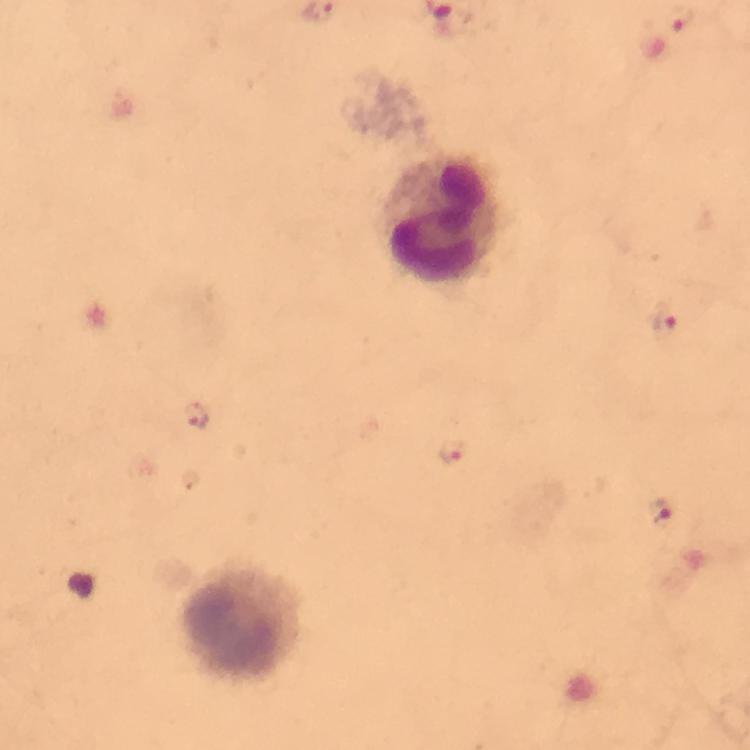
immersion oil = applied
context = from a malaria diagnostic workup
cropped from = a single field of view
image size = 750×750 pixels
stain = Giemsa
leukocyte locations = approximate centers as (x, y) in pixels: (440, 219), (245, 624)
preparation = thick blood smear
capture = smartphone photograph through a microscope
magnification = 100x
Plasmodium parasite locations = approximate centers as (x, y) in pixels: (682, 19), (668, 323), (197, 418), (452, 453), (660, 512)